Identify the cell.
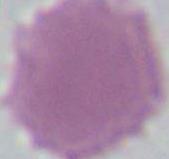
This is an erythrocyte.

1000x magnification. Photomicrograph.